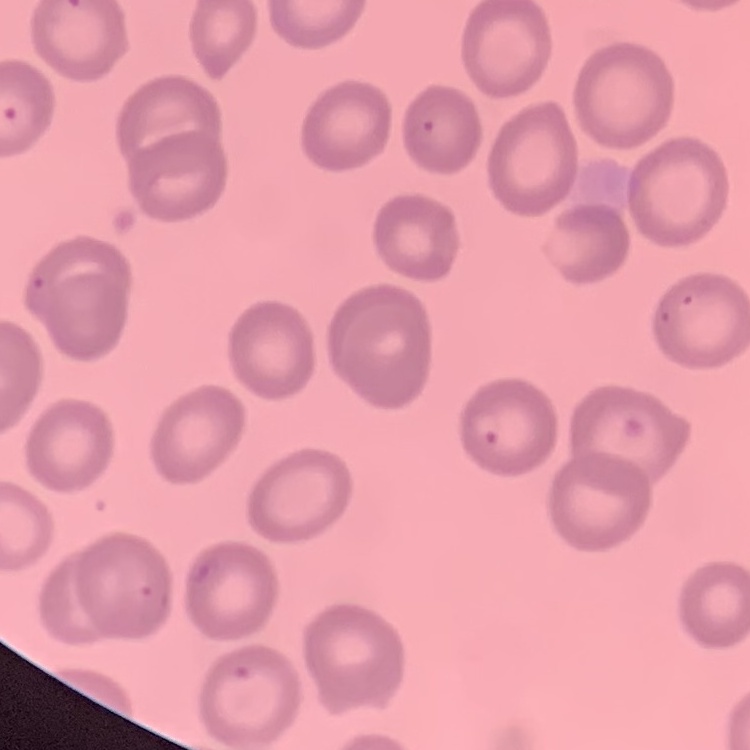

The red blood cells show no rouleaux formation. Square crop of a larger photomicrograph. Thin peripheral smear. Stained with either Field's or Giemsa.